Name the parasite shown.
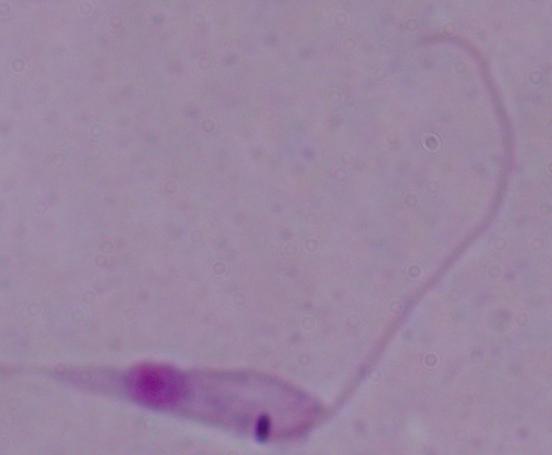

Leishmania.

magnification = 1000x
modality = micrograph